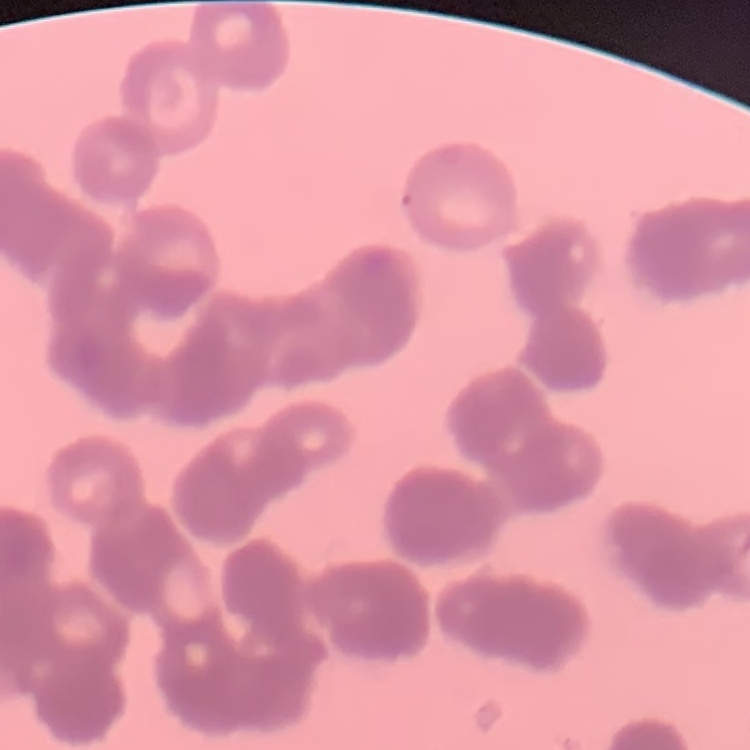
The red blood cells exhibit rouleaux formation. Stained with either Field's or Giemsa. Thin blood smear. Square crop of a larger photomicrograph.